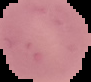

image size = 91×82 pixels
image type = cell region segmented out of the field of view; surrounding area masked to black
preparation = thin blood film
result = negative for Plasmodium parasites